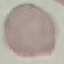

Result: no malaria parasites detected. Giemsa stain. Photographed with a smartphone camera at the microscope eyepiece. Cell patch, automatically extracted from a larger field of view and resized to 64 × 64 pixels. Thin blood film.